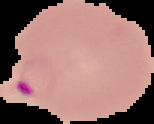

Summary:
  - Image type: segmented cell region with the area outside set to black
  - Image size: 154×124 pixels
  - Malaria status: parasitized
  - Preparation: thin blood film